Locate platelets.
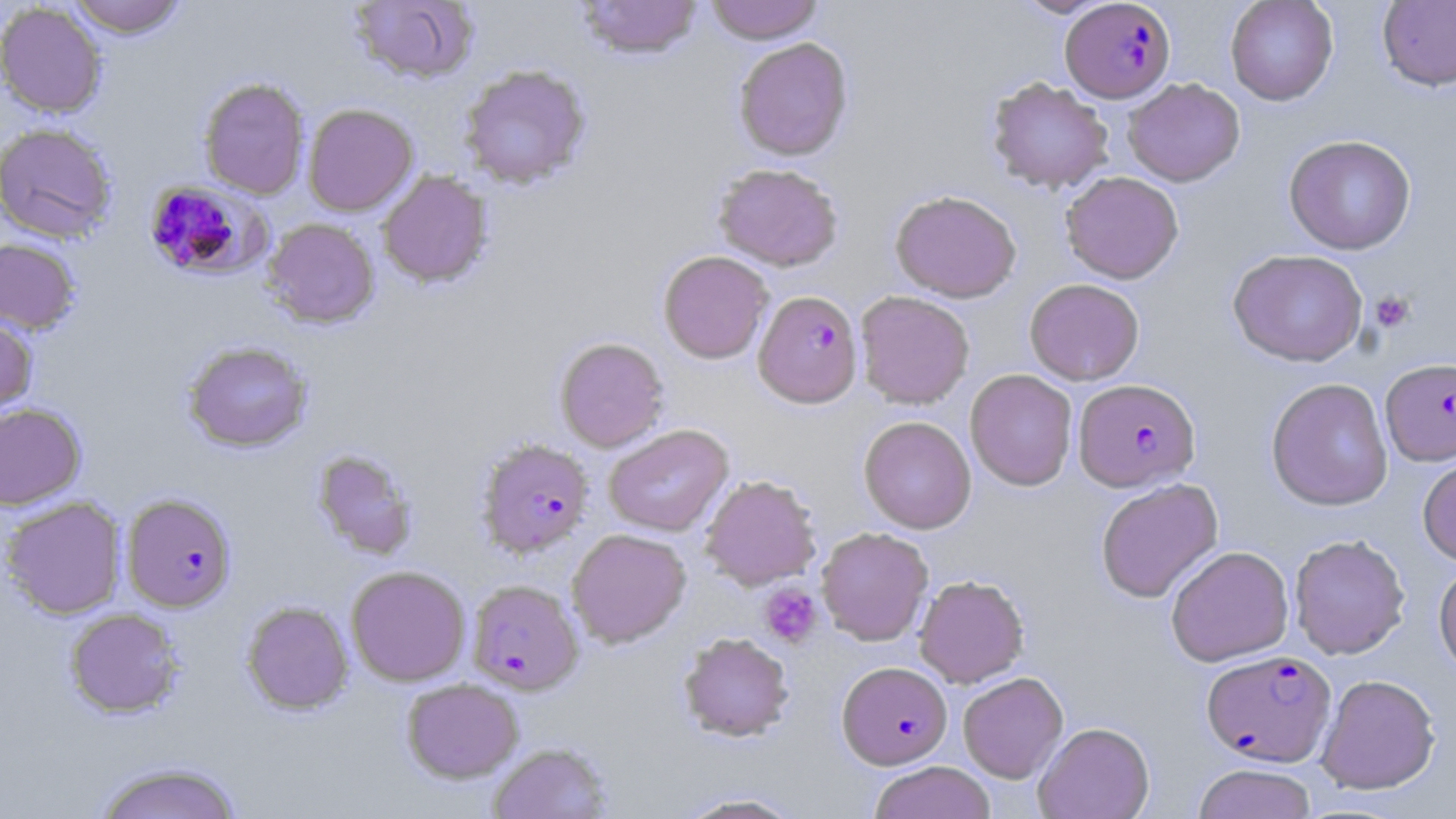

Approximate bounding boxes as (x1,y1)-(x2,y2) corner pairs in pixels.
Platelets: (1369,290)-(1416,333), (759,584)-(822,648).

Plasmodium falciparum-infected red blood cell locations: (1061,0)-(1174,102), (149,180)-(286,282), (753,290)-(863,408), (1380,358)-(1456,466), (1073,378)-(1200,492), (476,438)-(594,558), (122,493)-(237,612), (466,579)-(584,694), (1201,649)-(1336,766), (837,661)-(952,768). Uninfected red blood cell locations: (66,0)-(188,38), (348,0)-(479,85), (575,0)-(704,60), (705,0)-(823,44), (1013,0)-(1113,18), (1225,0)-(1338,105), (1377,1)-(1456,91), (0,2)-(108,117), (733,37)-(853,160), (458,64)-(592,189), (198,77)-(310,200), (986,77)-(1114,194), (1123,78)-(1245,186), (303,103)-(418,216), (0,122)-(119,244), (1283,134)-(1416,255), (712,163)-(844,271), (378,170)-(493,289), (1060,171)-(1184,284), (889,189)-(1022,302), (263,218)-(380,329), (0,237)-(81,334), (1228,249)-(1368,367), (658,250)-(774,364), (1024,279)-(1144,385), (855,291)-(975,409), (0,311)-(37,419), (554,336)-(669,452), (182,340)-(313,453), (965,369)-(1078,491), (1265,378)-(1393,511), (0,402)-(86,510), (859,416)-(976,534), (604,424)-(733,536), (311,448)-(419,561), (1417,452)-(1456,566), (699,474)-(822,590), (1096,478)-(1224,603), (1,496)-(126,619), (816,527)-(933,645), (567,528)-(691,647), (1289,534)-(1411,659), (1165,545)-(1294,667), (1433,561)-(1456,677), (346,565)-(471,686), (914,575)-(1029,688), (241,600)-(354,715), (64,608)-(184,717), (679,631)-(794,742), (958,672)-(1068,783), (1315,674)-(1440,794), (401,677)-(524,783), (1034,722)-(1155,819), (487,741)-(614,819), (92,760)-(245,819), (868,761)-(997,819), (1193,763)-(1318,819), (674,791)-(808,818). Slide-level diagnosis: Plasmodium falciparum. May-Grünwald-Giemsa-stained preparation. Captured at 1000x magnification. Light microscopy. Thin blood film. Image is 1456×819 pixels. One field of a larger specimen.